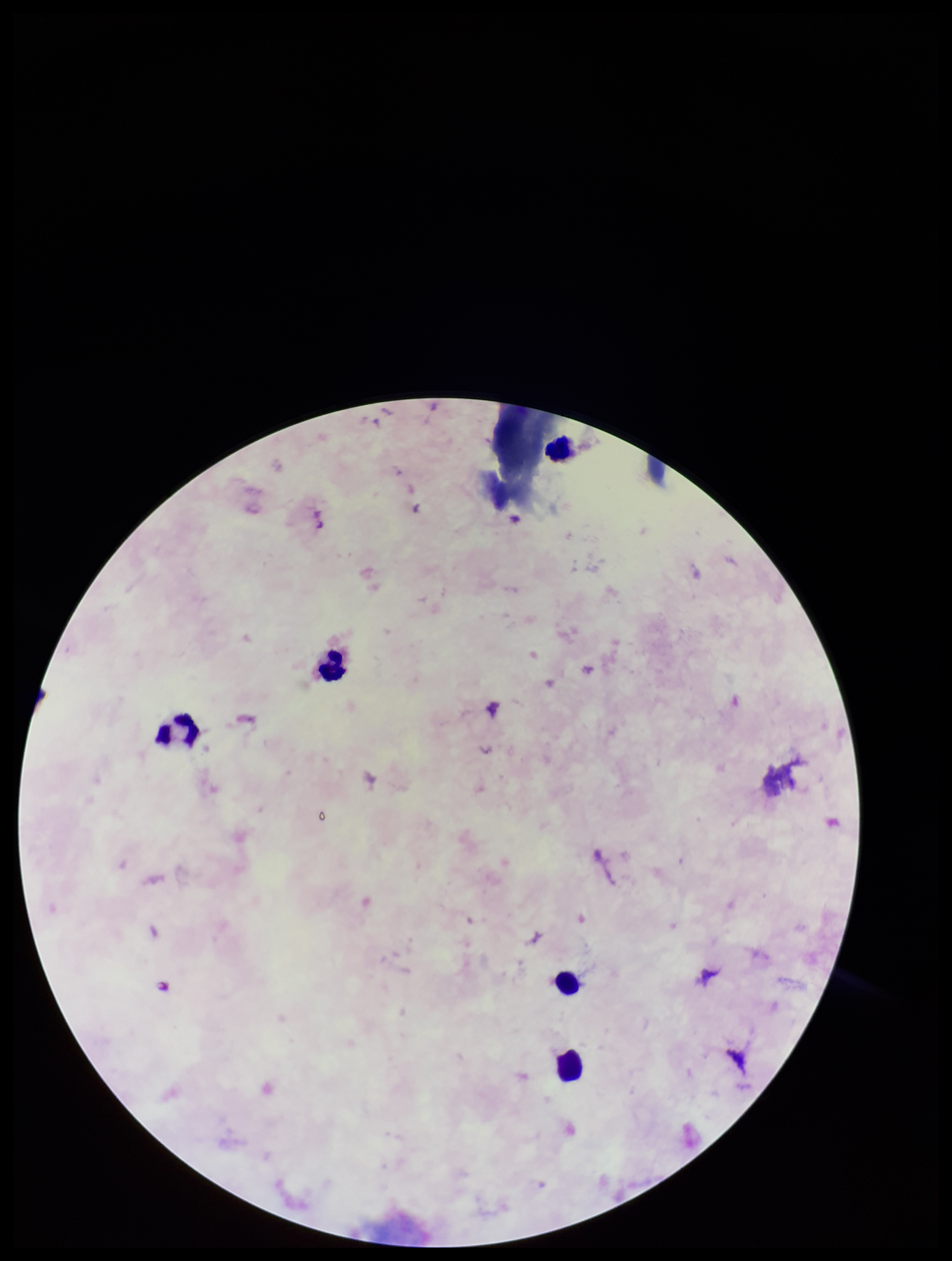
field of view = one from this slide
patient malaria status = negative
parasite count = 0
leukocyte count = 5
capture = smartphone photograph through the microscope eyepiece
preparation = thick blood smear
Plasmodium parasites = none identified
stain = Giemsa
image size = 952×1261 pixels